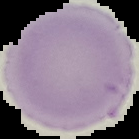
{
  "malaria_status": "uninfected",
  "preparation": "thin blood smear",
  "image_size": "139×139 pixels",
  "image_type": "segmented cell region on a black background"
}